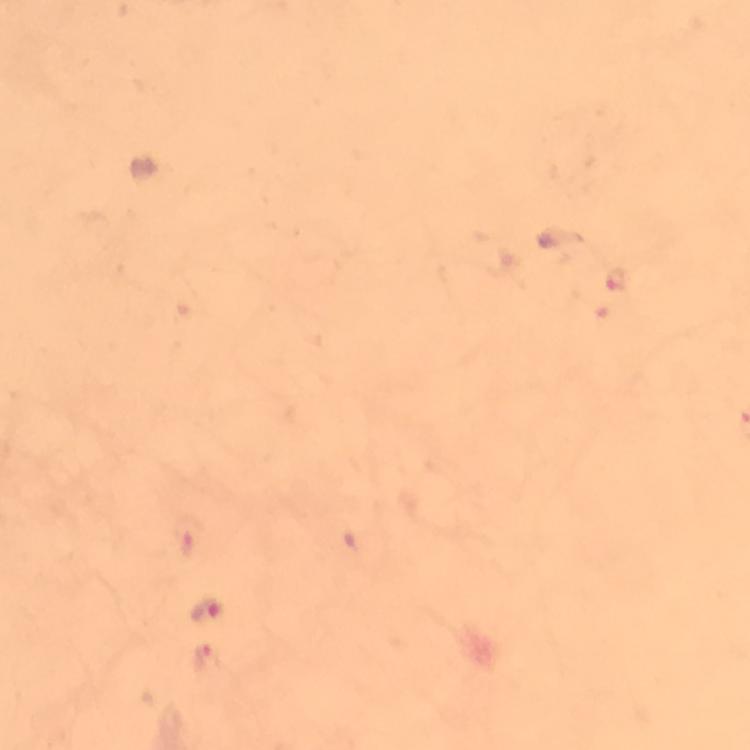

Approximate centers as {x, y} in pixels.
Summary:
  - Plasmodium parasite locations: {616, 279}, {188, 536}, {206, 611}, {207, 661}
  - Cropped from: a single field of view
  - Immersion oil: applied
  - Image size: 750×750 pixels
  - Stain: Giemsa
  - Context: from a diagnostic examination for malaria
  - Preparation: thick smear
  - Magnification: 100x
  - Capture: smartphone mounted on the microscope